Comment on the morphology of the erythrocytes.
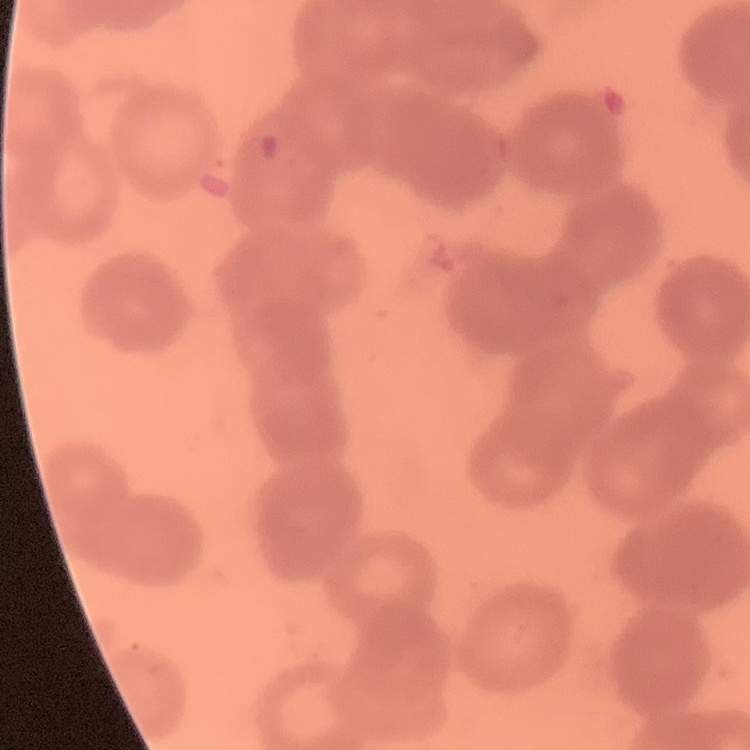

They show rouleaux formation.

Summary:
  - Image type: square crop of a larger photomicrograph
  - Preparation: thin blood smear
  - Stain: Field's or Giemsa